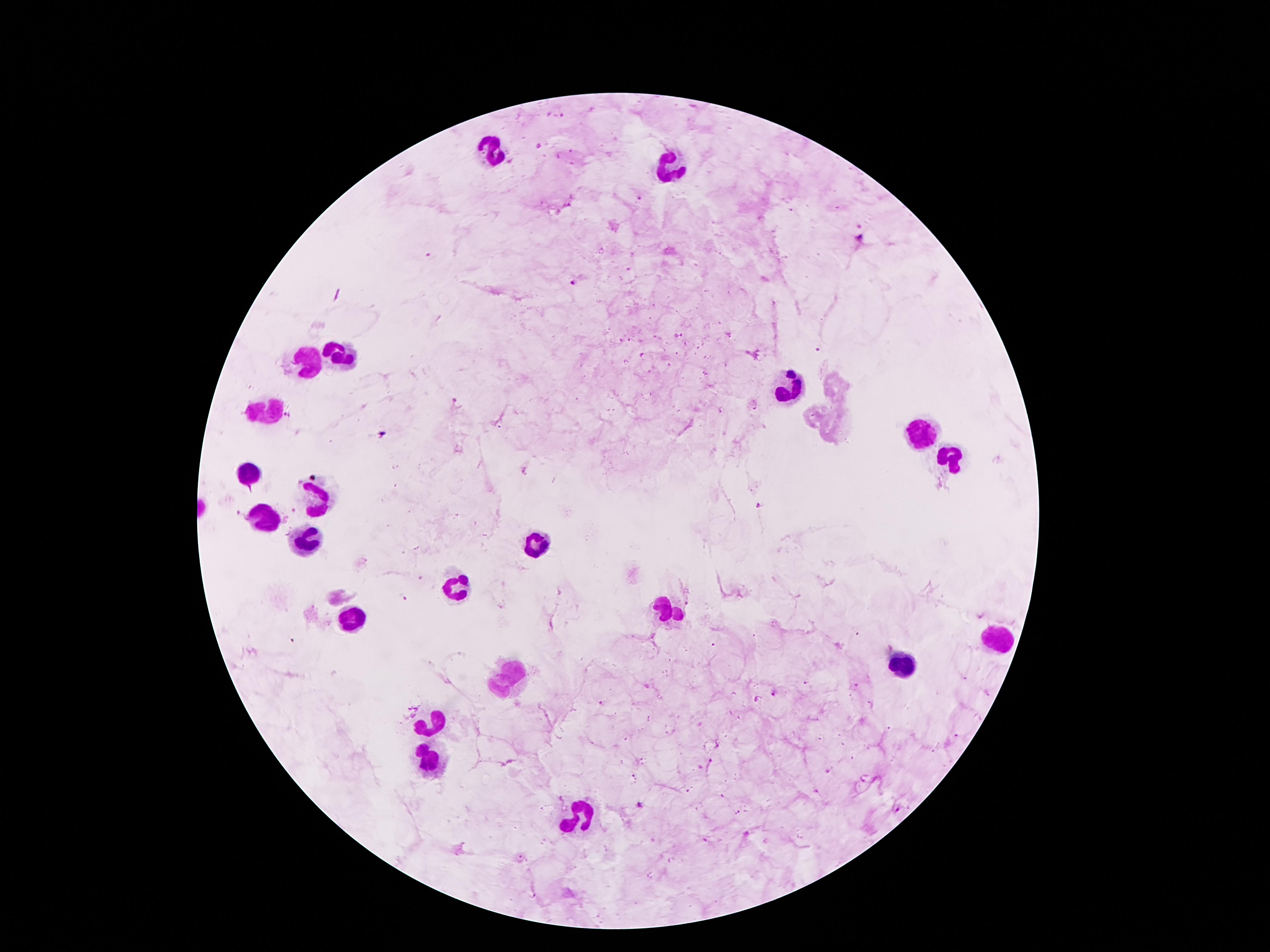

Approximate object centers, in pixels from the top-left corner. Leukocyte locations: (x=498, y=154), (x=670, y=165), (x=335, y=352), (x=307, y=362), (x=792, y=387), (x=263, y=412), (x=923, y=433), (x=954, y=457), (x=246, y=473), (x=316, y=497), (x=265, y=515), (x=305, y=534), (x=536, y=547), (x=450, y=587), (x=667, y=606), (x=356, y=614), (x=994, y=636), (x=902, y=664), (x=507, y=674), (x=432, y=723), (x=432, y=761), (x=577, y=818). Malaria parasite locations: (x=638, y=198), (x=859, y=238), (x=429, y=255), (x=574, y=281), (x=818, y=349), (x=456, y=404), (x=382, y=433), (x=758, y=507), (x=239, y=514), (x=407, y=599), (x=778, y=692), (x=600, y=702), (x=641, y=805). Thick blood film. Image is 1270×952 pixels. 100x magnification. Photographed through the microscope eyepiece with a smartphone camera. Giemsa stain. One field from this slide. Patient malaria status: positive for Plasmodium falciparum.